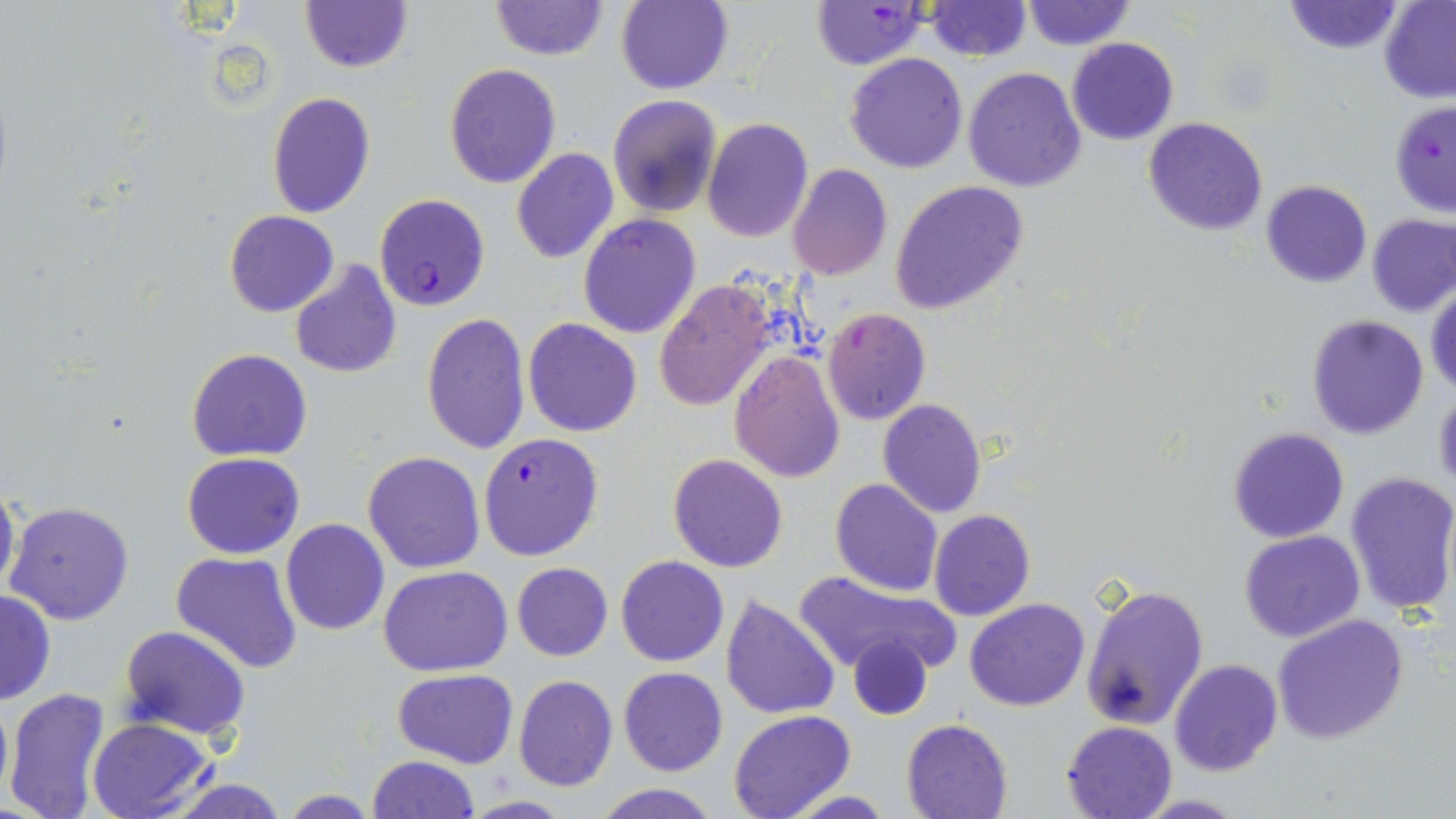

slide-level diagnosis = Plasmodium falciparum
image size = 1456×819 pixels
magnification = 1000x
preparation = thin blood film
modality = light microscopy
Plasmodium falciparum-infected red blood cell locations = approximate bounding boxes as [x1, y1, x2, y2] in pixels: [811, 1, 932, 71], [1389, 100, 1456, 218], [375, 193, 489, 311], [478, 432, 604, 559]
stain = May-Grünwald-Giemsa
field of view = single
uninfected red blood cell locations = approximate bounding boxes as [x1, y1, x2, y2] in pixels: [489, 0, 607, 61], [300, 1, 413, 73], [614, 1, 734, 93], [922, 1, 1031, 61], [1020, 1, 1133, 51], [1283, 1, 1402, 54], [1378, 1, 1456, 103], [1066, 37, 1179, 145], [844, 53, 968, 173], [443, 63, 561, 188], [963, 66, 1086, 192], [266, 91, 376, 219], [607, 94, 723, 218], [701, 117, 813, 241], [1143, 117, 1267, 237], [511, 146, 620, 265], [789, 164, 893, 281], [1260, 179, 1372, 286], [892, 182, 1029, 317], [224, 210, 337, 318], [578, 213, 703, 339], [1368, 214, 1456, 315], [289, 261, 403, 379], [654, 281, 779, 413], [1427, 286, 1456, 400], [823, 307, 932, 426], [420, 312, 531, 456], [1306, 314, 1430, 440], [522, 317, 642, 437], [186, 348, 312, 461], [728, 349, 846, 482], [1434, 385, 1456, 496], [877, 399, 987, 518], [1228, 426, 1349, 543], [362, 451, 487, 573], [182, 452, 306, 559], [667, 453, 788, 573], [1343, 471, 1456, 620], [1, 478, 20, 602], [830, 478, 943, 597], [6, 501, 132, 626], [930, 510, 1035, 621], [280, 519, 389, 636], [1239, 530, 1365, 643], [171, 551, 303, 673], [616, 555, 729, 668], [512, 562, 613, 661], [378, 564, 514, 676], [793, 566, 961, 679], [1081, 583, 1208, 730], [0, 590, 56, 704], [719, 591, 840, 720], [965, 597, 1090, 712], [1272, 613, 1408, 743], [118, 625, 251, 742], [845, 632, 935, 721], [1169, 658, 1282, 777], [619, 666, 728, 777], [393, 668, 519, 768], [513, 674, 618, 791], [4, 688, 111, 819], [0, 689, 12, 812], [727, 710, 856, 819], [86, 717, 215, 819], [901, 718, 1015, 819], [1061, 720, 1178, 819], [367, 754, 480, 819], [165, 779, 291, 818], [590, 782, 722, 818], [785, 790, 896, 818], [457, 796, 576, 818]